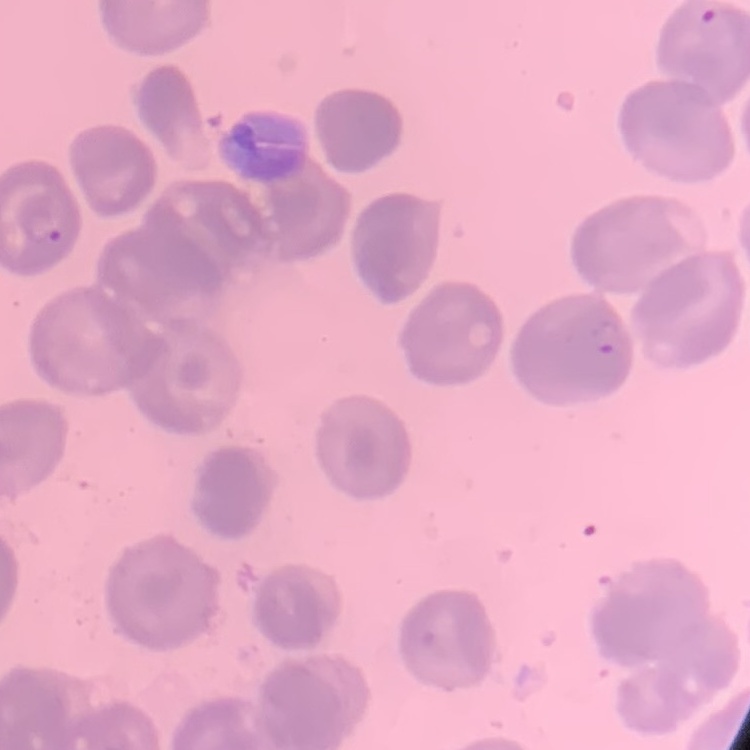
{
  "red_blood_cell_morphology": "no rouleaux formation",
  "preparation": "thin peripheral smear",
  "stain": "Field's or Giemsa",
  "image_type": "square crop of a larger photomicrograph"
}